Assess this cell for malaria.
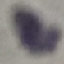
Uninfected.

stain = Giemsa
preparation = thin blood film
capture = smartphone through the microscope eyepiece
image type = cell patch, automatically extracted from a larger field of view and resized to 64 × 64 pixels